Outline each white blood cell.
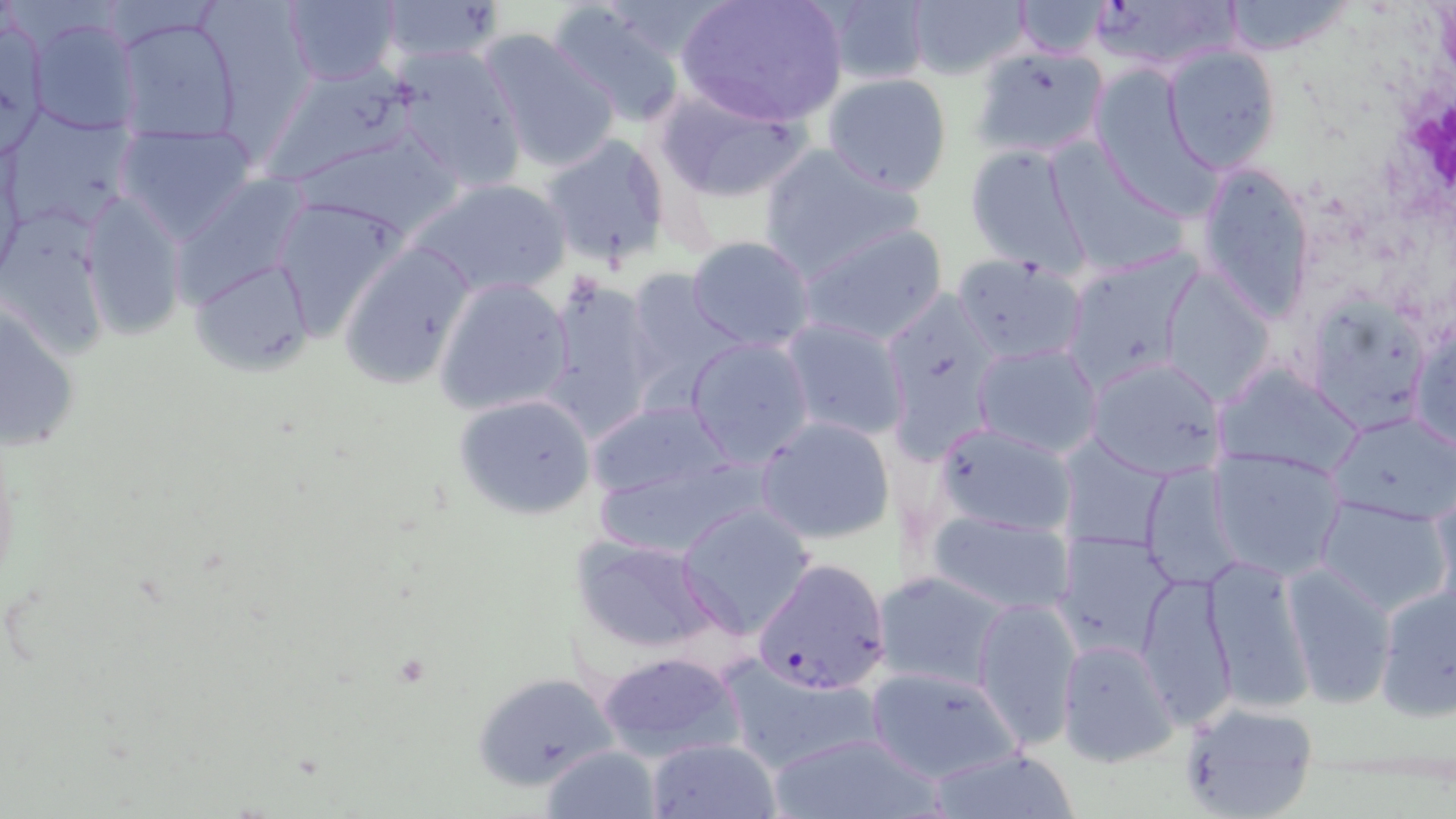

Approximate bounding boxes as (x1,y1)-(x2,y2) corner pairs in pixels.
White blood cells: (1389,66)-(1453,214).

slide-level diagnosis = Plasmodium falciparum
modality = light microscopy
uninfected red blood cell locations = approximate bounding boxes as (x1,y1)-(x2,y2) corner pairs in pixels: (281,0)-(402,88), (677,0)-(849,127), (811,0)-(933,89), (1220,0)-(1352,57), (372,1)-(509,68), (908,1)-(1029,80), (1012,1)-(1115,59), (547,2)-(690,129), (0,13)-(47,154), (23,15)-(141,135), (112,15)-(242,145), (475,27)-(621,173), (1161,45)-(1284,174), (392,47)-(526,192), (972,47)-(1110,160), (260,60)-(431,185), (822,73)-(953,195), (651,82)-(815,202), (4,110)-(137,235), (116,122)-(261,242), (291,128)-(463,238), (539,132)-(674,273), (965,143)-(1092,273), (757,144)-(924,279), (1045,144)-(1188,276), (0,146)-(26,288), (1195,160)-(1316,323), (170,173)-(312,313), (406,176)-(569,301), (79,191)-(186,340), (270,195)-(413,338), (1,203)-(110,360), (795,223)-(950,348), (686,236)-(816,352), (336,237)-(477,390), (1063,250)-(1199,390), (952,253)-(1087,364), (186,254)-(313,376), (1160,268)-(1275,404), (620,272)-(746,409), (434,275)-(575,416), (541,276)-(660,439), (1304,287)-(1425,430), (2,294)-(81,456), (1410,318)-(1455,452), (779,319)-(912,442), (686,337)-(815,467), (973,342)-(1102,459), (1087,357)-(1223,479), (1213,361)-(1364,478), (453,392)-(598,522), (583,397)-(740,506), (1329,411)-(1456,525), (755,417)-(895,545), (936,423)-(1076,537), (1209,446)-(1347,578), (592,454)-(766,558), (1142,461)-(1241,590), (1429,483)-(1456,605), (1318,496)-(1450,615), (678,503)-(816,640), (924,507)-(1075,612), (1053,528)-(1178,663), (570,535)-(719,655), (1200,553)-(1313,712), (1280,564)-(1399,706), (874,570)-(1012,691), (1136,571)-(1237,727), (1375,580)-(1456,721), (973,595)-(1081,750), (1054,637)-(1177,769), (595,649)-(746,757), (718,652)-(883,776), (863,664)-(1023,784), (471,670)-(625,791), (1175,699)-(1319,819), (764,731)-(946,819), (646,737)-(780,818), (542,744)-(661,817), (926,744)-(1081,819)
Plasmodium falciparum-infected red blood cell locations = approximate bounding boxes as (x1,y1)-(x2,y2) corner pairs in pixels: (1082,0)-(1246,73), (751,560)-(891,695)
preparation = thin blood film
image size = 1456×819 pixels
stain = May-Grünwald-Giemsa
magnification = 1000x
field of view = single